Assess this cell for malaria.
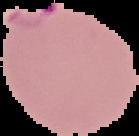

Parasitized.

{
  "image_type": "segmented cell region on a black background",
  "image_size": "139×136 pixels",
  "preparation": "thin blood smear"
}